Locate every blood parasite and identify its species.
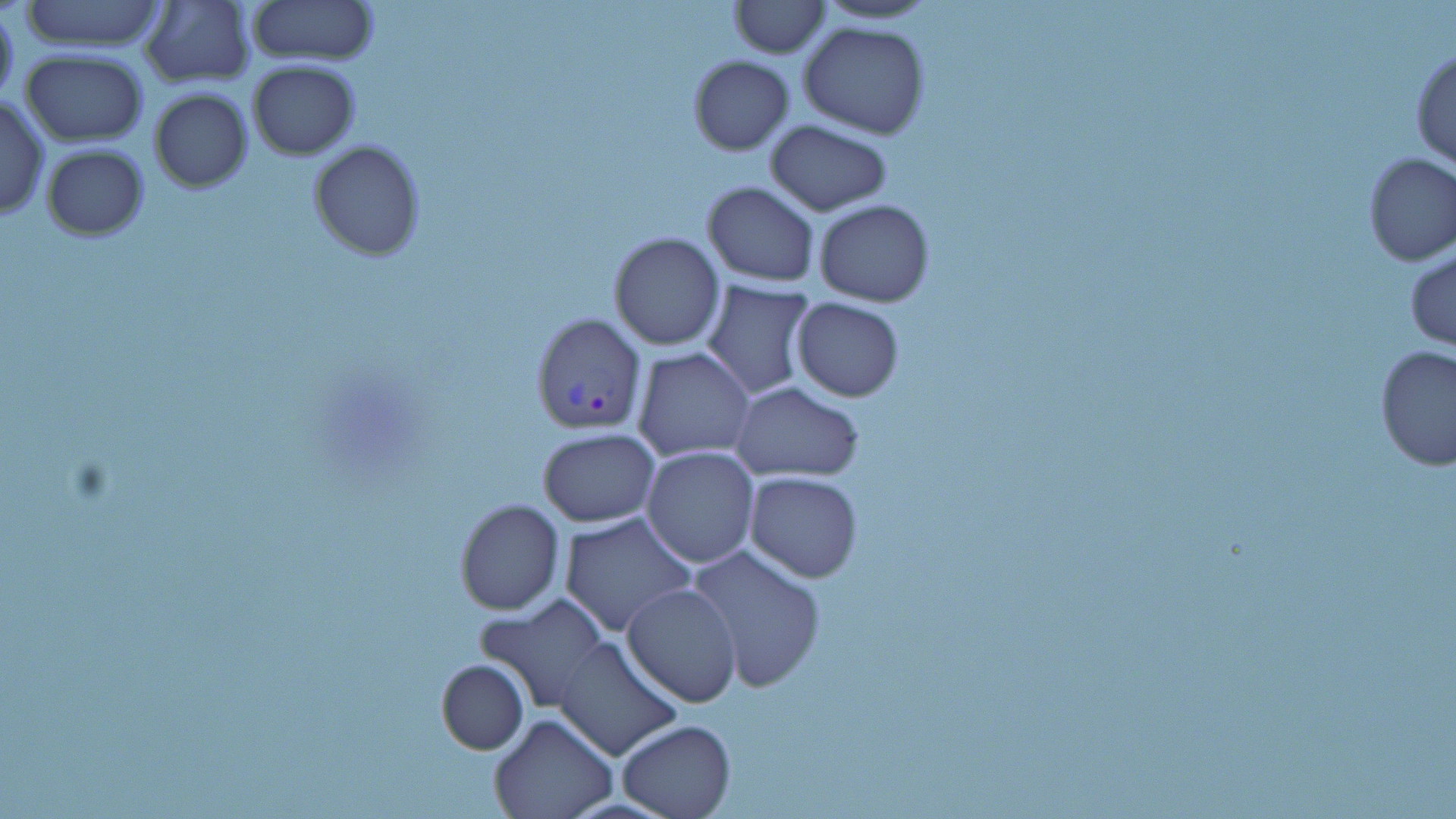
Approximate bounding boxes as [x1, y1, x2, y2] in pixels.
Plasmodium vivax-infected red blood cells: [532, 313, 648, 435].
No Plasmodium falciparum, Plasmodium ovale, Plasmodium malariae, Babesia divergens, or Trypanosoma brucei observed.

slide-level diagnosis = Plasmodium vivax
uninfected red blood cell locations = approximate bounding boxes as [x1, y1, x2, y2] in pixels: [20, 0, 169, 53], [246, 0, 379, 67], [728, 0, 829, 57], [810, 0, 943, 26], [139, 2, 256, 86], [0, 8, 19, 107], [798, 20, 930, 138], [1411, 48, 1456, 172], [20, 50, 148, 145], [689, 55, 794, 154], [248, 61, 360, 159], [149, 88, 253, 192], [0, 95, 49, 220], [764, 121, 893, 214], [309, 140, 424, 259], [41, 143, 149, 240], [1361, 152, 1456, 266], [700, 181, 820, 286], [814, 200, 934, 307], [609, 232, 725, 351], [1405, 249, 1455, 352], [699, 280, 819, 400], [790, 298, 905, 401], [1375, 344, 1456, 472], [632, 346, 755, 461], [730, 382, 864, 482], [537, 428, 660, 528], [641, 445, 760, 567], [745, 472, 863, 582], [454, 498, 564, 615], [558, 513, 697, 639], [685, 544, 828, 692], [623, 582, 743, 705], [475, 595, 611, 711], [553, 635, 681, 761], [436, 659, 528, 754], [489, 711, 618, 819], [616, 720, 738, 819]
image size = 1456×819 pixels
preparation = thin blood film
magnification = 1000x
modality = optical microscopy
stain = May-Grünwald-Giemsa
field of view = single